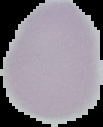
image size = 103×127 pixels
preparation = thin blood smear
image type = segmented cell region on a black background
malaria status = uninfected